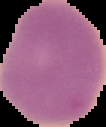

Image is 106×127 pixels. Cell region segmented out of the field of view; the surrounding area is masked to black. Malaria status: uninfected. From a thin blood smear.